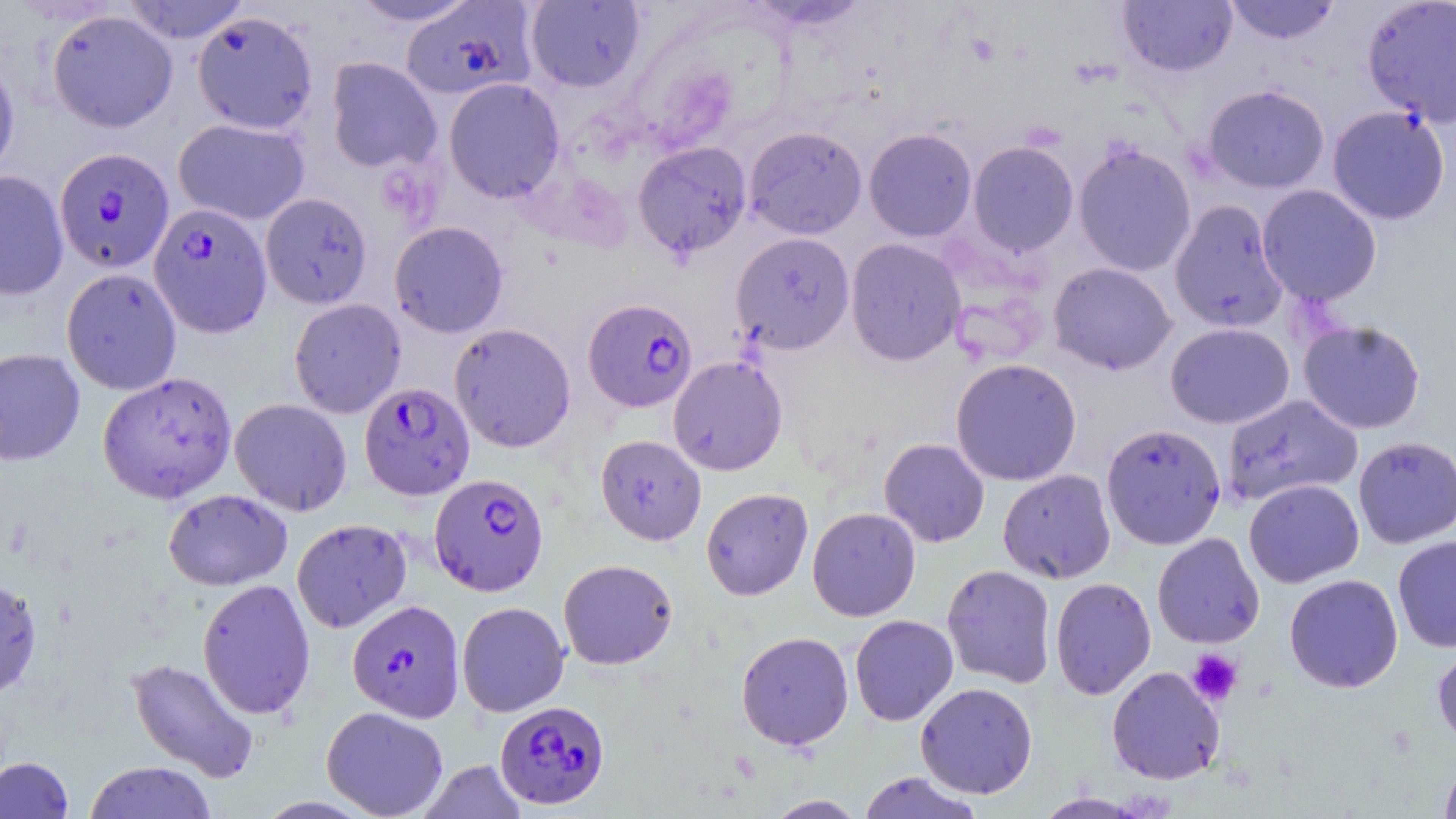
slide_level_diagnosis: Plasmodium falciparum
magnification: 1000x
uninfected_red_blood_cell_locations: 'approximate bounding boxes as named x1/y1/x2/y2 corners in pixels: (x1=119, y1=0, x2=252, y2=44), (x1=346, y1=0, x2=482, y2=27), (x1=745, y1=0, x2=873, y2=32), (x1=1224, y1=0, x2=1341, y2=45), (x1=1362, y1=0, x2=1456, y2=127), (x1=525, y1=1, x2=645, y2=92), (x1=1118, y1=1, x2=1237, y2=77), (x1=47, y1=9, x2=178, y2=133), (x1=192, y1=10, x2=319, y2=134), (x1=0, y1=54, x2=20, y2=181), (x1=326, y1=57, x2=442, y2=174), (x1=444, y1=77, x2=564, y2=203), (x1=1202, y1=84, x2=1330, y2=193), (x1=1327, y1=106, x2=1450, y2=225), (x1=173, y1=118, x2=310, y2=225), (x1=743, y1=126, x2=868, y2=239), (x1=863, y1=128, x2=977, y2=242), (x1=968, y1=140, x2=1079, y2=255), (x1=632, y1=141, x2=752, y2=258), (x1=1073, y1=141, x2=1197, y2=276), (x1=0, y1=171, x2=69, y2=301), (x1=1257, y1=184, x2=1382, y2=306), (x1=260, y1=192, x2=372, y2=309), (x1=1169, y1=199, x2=1288, y2=333), (x1=390, y1=221, x2=508, y2=338), (x1=730, y1=232, x2=855, y2=355), (x1=845, y1=238, x2=966, y2=366), (x1=1048, y1=262, x2=1177, y2=375), (x1=61, y1=267, x2=182, y2=395), (x1=289, y1=298, x2=406, y2=418), (x1=1298, y1=319, x2=1426, y2=435), (x1=449, y1=322, x2=576, y2=453), (x1=1165, y1=322, x2=1295, y2=429), (x1=0, y1=348, x2=85, y2=466), (x1=668, y1=355, x2=788, y2=476), (x1=950, y1=358, x2=1082, y2=486), (x1=98, y1=371, x2=237, y2=503), (x1=1222, y1=394, x2=1363, y2=506), (x1=230, y1=398, x2=352, y2=516), (x1=1101, y1=423, x2=1226, y2=549), (x1=595, y1=434, x2=706, y2=545), (x1=1353, y1=436, x2=1456, y2=548), (x1=879, y1=438, x2=990, y2=547), (x1=998, y1=469, x2=1117, y2=584), (x1=1244, y1=478, x2=1364, y2=588), (x1=700, y1=487, x2=814, y2=600), (x1=163, y1=489, x2=293, y2=591), (x1=807, y1=507, x2=921, y2=621), (x1=291, y1=518, x2=412, y2=633), (x1=1152, y1=532, x2=1265, y2=649), (x1=1393, y1=535, x2=1456, y2=652), (x1=558, y1=559, x2=678, y2=670), (x1=941, y1=564, x2=1056, y2=687), (x1=1284, y1=574, x2=1403, y2=693), (x1=0, y1=576, x2=42, y2=700), (x1=1050, y1=577, x2=1156, y2=700), (x1=197, y1=578, x2=316, y2=719), (x1=456, y1=601, x2=570, y2=717), (x1=850, y1=614, x2=959, y2=726), (x1=736, y1=630, x2=854, y2=750), (x1=1432, y1=642, x2=1456, y2=749), (x1=126, y1=657, x2=260, y2=782), (x1=1106, y1=666, x2=1225, y2=784), (x1=915, y1=682, x2=1038, y2=799), (x1=321, y1=705, x2=448, y2=819), (x1=1439, y1=754, x2=1456, y2=819), (x1=0, y1=757, x2=74, y2=818), (x1=418, y1=760, x2=527, y2=819), (x1=83, y1=761, x2=217, y2=819), (x1=858, y1=771, x2=983, y2=819), (x1=1034, y1=792, x2=1150, y2=818), (x1=763, y1=794, x2=868, y2=818)'
platelet_locations: 'approximate bounding boxes as named x1/y1/x2/y2 corners in pixels: (x1=1187, y1=649, x2=1243, y2=706)'
preparation: thin blood smear
image_size: 1456×819 pixels
field_of_view: single
modality: light microscopy
stain: May-Grünwald-Giemsa
plasmodium_falciparum_infected_red_blood_cell_locations: 'approximate bounding boxes as named x1/y1/x2/y2 corners in pixels: (x1=401, y1=2, x2=536, y2=99), (x1=55, y1=147, x2=174, y2=272), (x1=149, y1=202, x2=272, y2=337), (x1=583, y1=297, x2=697, y2=412), (x1=359, y1=381, x2=475, y2=501), (x1=429, y1=473, x2=549, y2=596), (x1=347, y1=599, x2=465, y2=722), (x1=495, y1=700, x2=609, y2=810)'